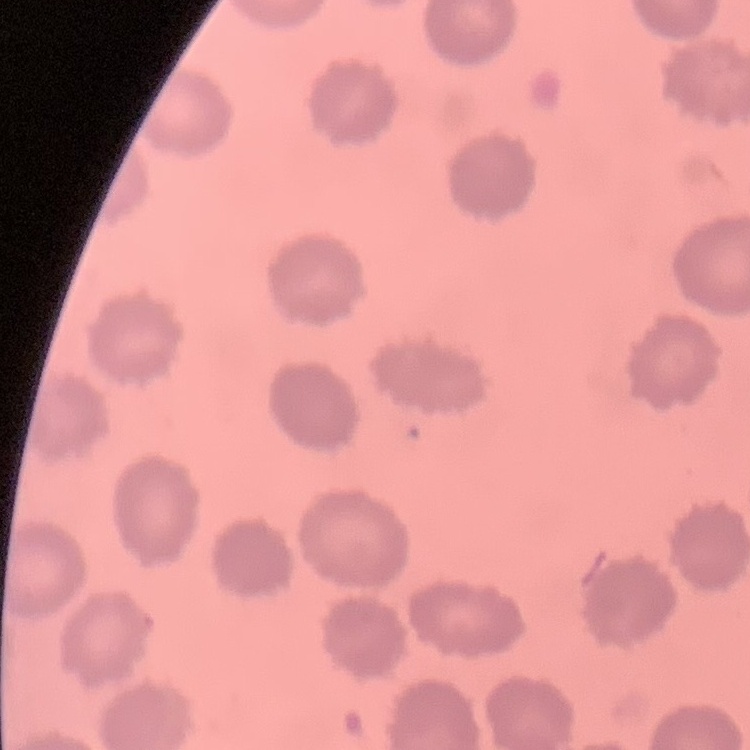

Summary:
  - Erythrocyte morphology: no rouleaux formation
  - Image type: one tile cut from a larger photomicrograph
  - Preparation: thin peripheral smear
  - Stain: Field's or Giemsa